Describe the morphology of the red blood cells.
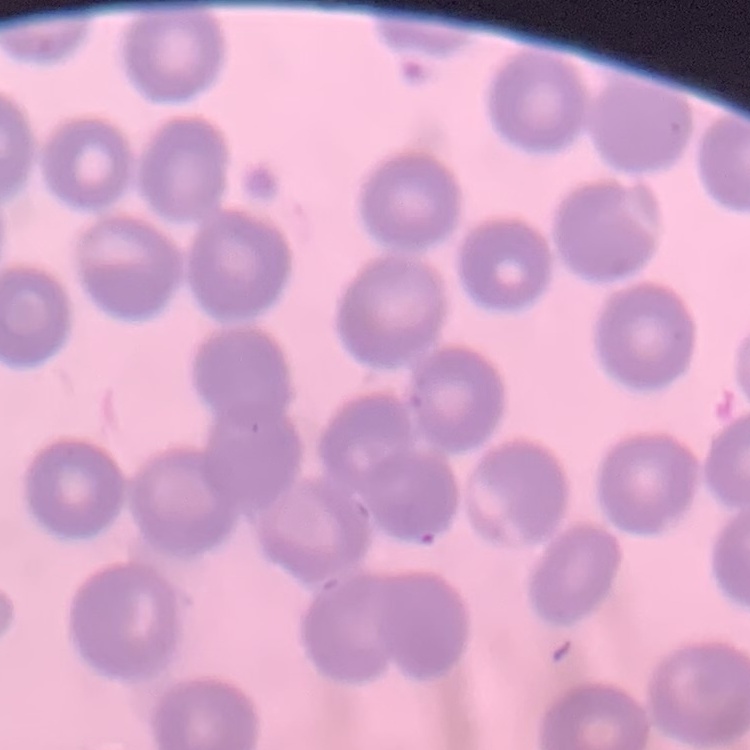

No rouleaux formation.

stain = Field's or Giemsa
image type = square crop of a larger photomicrograph
preparation = thin blood smear